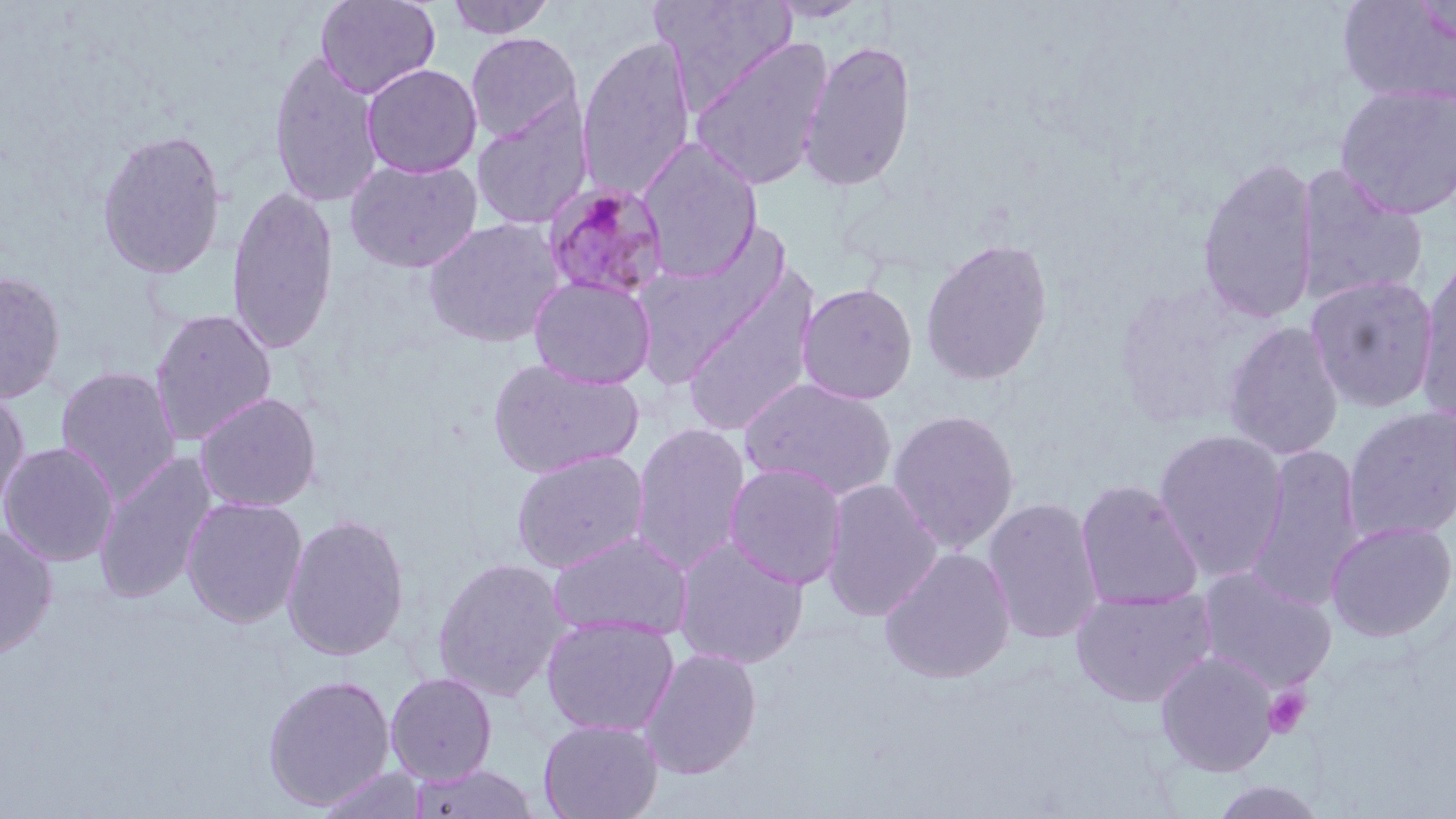

Summary:
  - Coordinate format: approximate bounding boxes as (x1,y1)-(x2,y2) corner pairs in pixels
  - Platelet locations: (1263,687)-(1310,738)
  - Plasmodium malariae-infected red blood cell locations: (543,180)-(671,303)
  - Uninfected red blood cell locations: (315,0)-(440,99), (444,0)-(557,39), (650,0)-(798,109), (766,0)-(872,24), (1337,1)-(1456,107), (465,31)-(584,144), (577,34)-(697,201), (689,37)-(833,191), (798,38)-(917,192), (268,48)-(384,209), (362,63)-(482,178), (1334,83)-(1456,220), (470,99)-(593,230), (96,127)-(228,279), (638,139)-(762,282), (1197,154)-(1319,325), (345,158)-(483,273), (1296,165)-(1429,307), (226,184)-(340,356), (423,217)-(564,348), (919,237)-(1054,386), (1415,259)-(1456,427), (681,269)-(820,438), (0,270)-(66,405), (1306,273)-(1440,413), (529,276)-(656,390), (796,282)-(918,405), (150,307)-(278,445), (1223,321)-(1344,460), (486,358)-(643,479), (55,365)-(182,504), (740,378)-(897,501), (0,388)-(30,516), (194,391)-(322,512), (1342,406)-(1456,544), (887,409)-(1020,553), (630,422)-(751,575), (1152,429)-(1289,582), (0,441)-(120,567), (1246,444)-(1366,612), (510,449)-(649,573), (93,452)-(217,606), (724,462)-(848,590), (821,479)-(943,621), (1075,479)-(1204,611), (181,496)-(308,628), (982,496)-(1105,645), (281,514)-(410,661), (1325,520)-(1455,642), (0,524)-(58,659), (548,531)-(692,642), (673,537)-(809,670), (879,547)-(1016,684), (433,557)-(570,701), (1197,568)-(1338,694), (1070,587)-(1217,708), (541,615)-(680,737), (638,647)-(762,779), (1154,650)-(1279,777), (385,672)-(498,785), (262,674)-(396,810), (538,719)-(663,819), (410,763)-(538,819), (314,766)-(429,819), (1209,779)-(1330,818)
  - Slide-level diagnosis: Plasmodium malariae
  - Modality: light microscopy
  - Stain: May-Grünwald-Giemsa
  - Image size: 1456×819 pixels
  - Preparation: thin blood film
  - Field of view: single
  - Magnification: 1000x